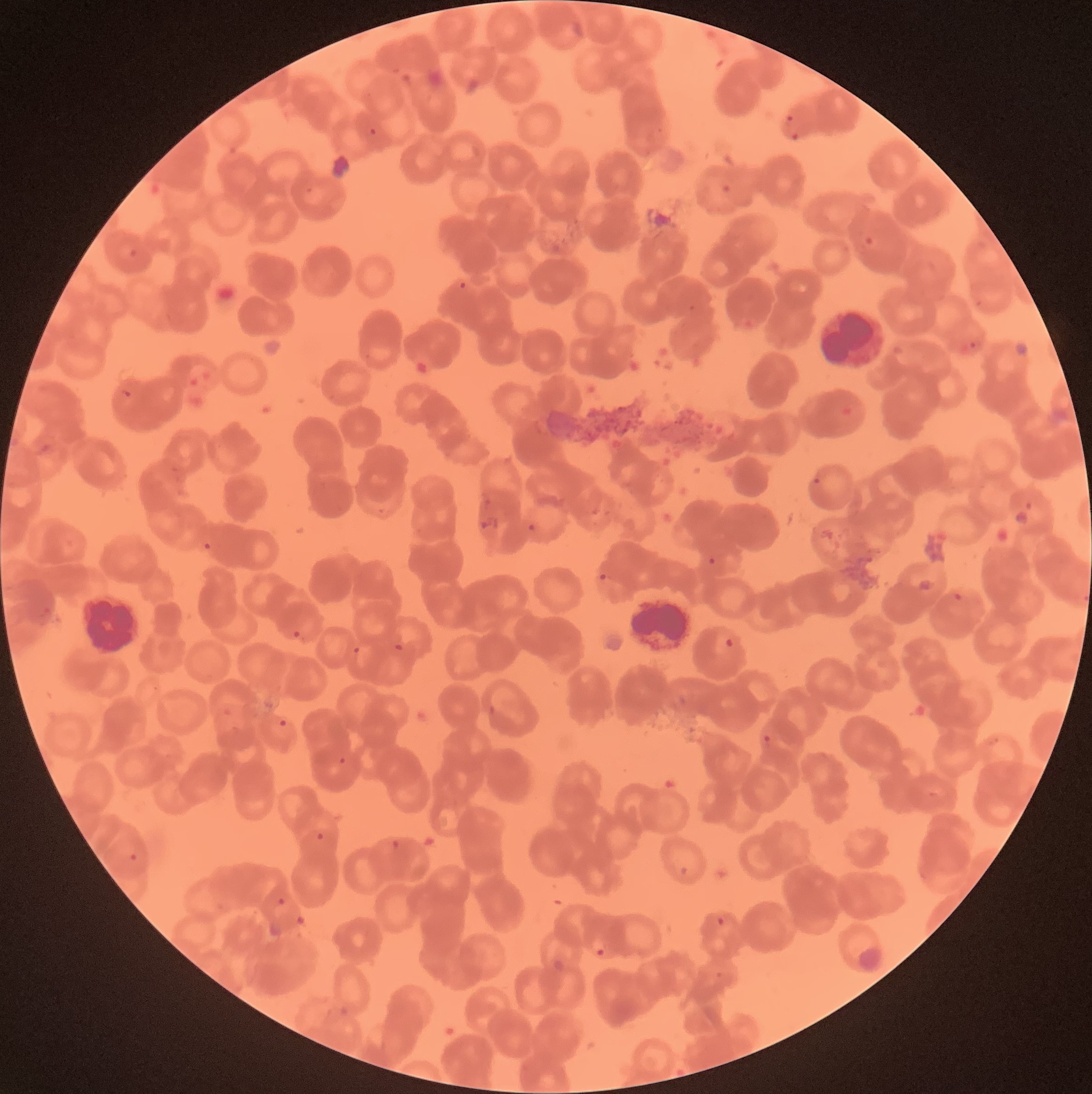 Approximate bounding boxes as (x1, y1, x2, y2) in pixels. Plasmodium parasite locations: (786, 114, 799, 140), (368, 127, 377, 137), (721, 183, 732, 195), (862, 233, 878, 251), (129, 247, 138, 258), (457, 278, 470, 293), (960, 339, 982, 355), (118, 387, 133, 400), (811, 476, 823, 488), (1024, 502, 1033, 510), (478, 511, 500, 530), (527, 522, 539, 533), (203, 542, 212, 552), (707, 556, 717, 566), (597, 570, 609, 584), (951, 591, 964, 603), (292, 629, 301, 640), (722, 636, 735, 650), (393, 642, 405, 653), (353, 646, 361, 654), (278, 717, 288, 729), (762, 734, 774, 749), (338, 756, 346, 765), (316, 832, 325, 842), (391, 839, 400, 848), (128, 852, 138, 861), (679, 864, 689, 878), (277, 897, 286, 906), (716, 915, 725, 926), (596, 948, 605, 957). White blood cell locations: (78, 593, 147, 656), (630, 598, 690, 655). Image is 1092×1094 pixels. Optical microscopy. Thin blood film. The red blood cells show rouleaux formation.